Look for Plasmodium parasites.
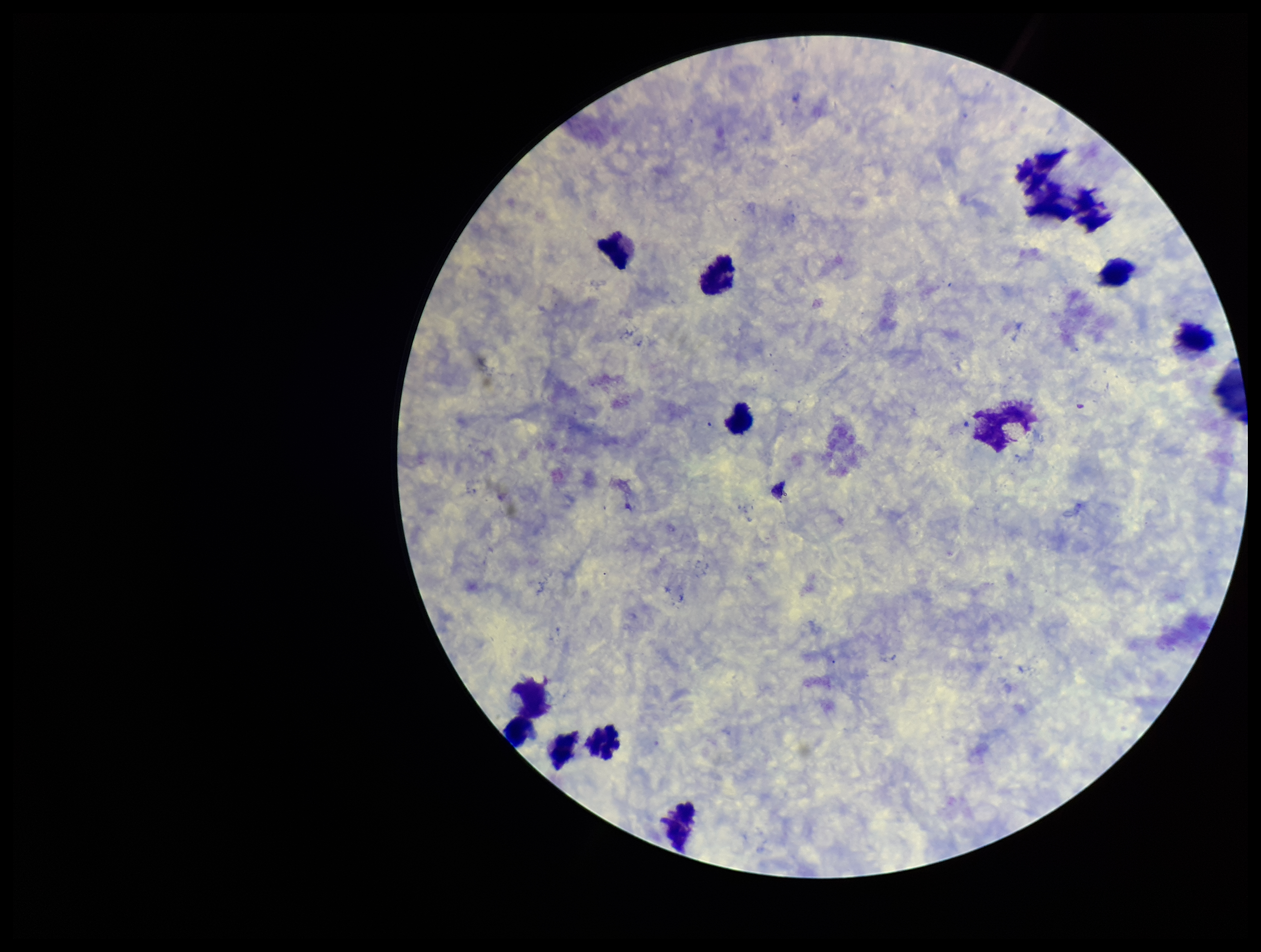

None identified.

{
  "image_size": "1261×952 pixels",
  "leukocyte_count": 12,
  "parasite_count": 0,
  "field_of_view": "single",
  "stain": "Giemsa",
  "preparation": "thick smear",
  "capture": "smartphone photograph through the microscope eyepiece",
  "patient_malaria_status": "negative"
}